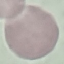
Result: no malaria parasites detected. Automatically extracted cell patch, resized to 64 × 64 pixels. Acquired by smartphone through the microscope eyepiece. Thin blood smear. Giemsa stain.